Report the malaria status of this cell.
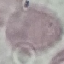

It is uninfected.

Automatically extracted cell patch, resized to 64 × 64 pixels. Giemsa stain. Photographed with a smartphone camera at the microscope eyepiece. Thin blood smear.